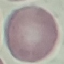

Result: negative for malaria parasites. Thin blood smear. Cell patch, automatically extracted from a larger field of view and resized to 64 × 64 pixels. Giemsa-stained preparation. Photographed with a smartphone camera at the microscope eyepiece.